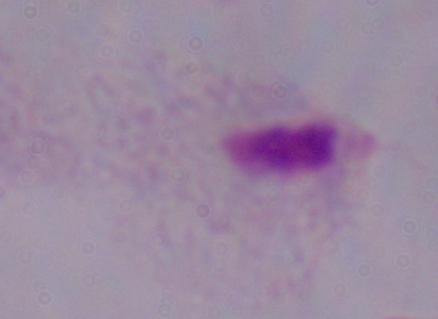
Summary:
  - Identification: trichomonad
  - Magnification: 1000x
  - Modality: micrograph